Name the parasite shown.
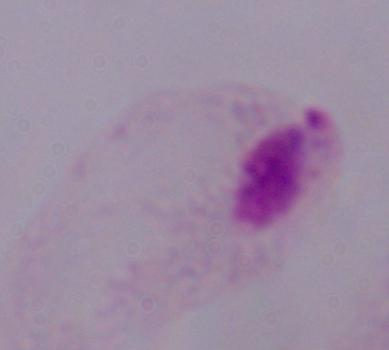

This is a trichomonad.

Summary:
  - Magnification: 1000x
  - Modality: micrograph